Comment on the morphology of the erythrocytes.
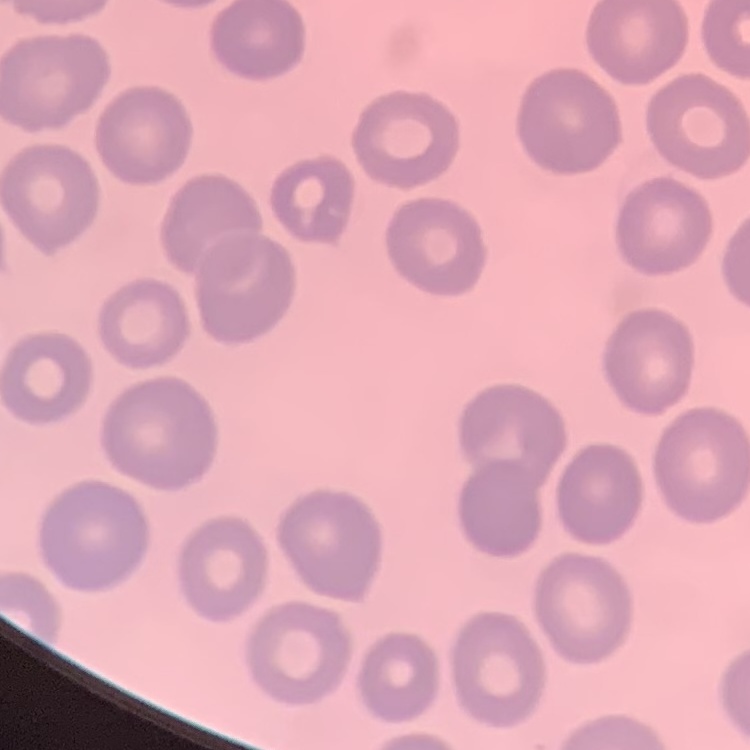
They show no rouleaux formation.

Square crop of a larger photomicrograph. Thin blood smear. Stained with either Field's or Giemsa.